State the blood parasite species.
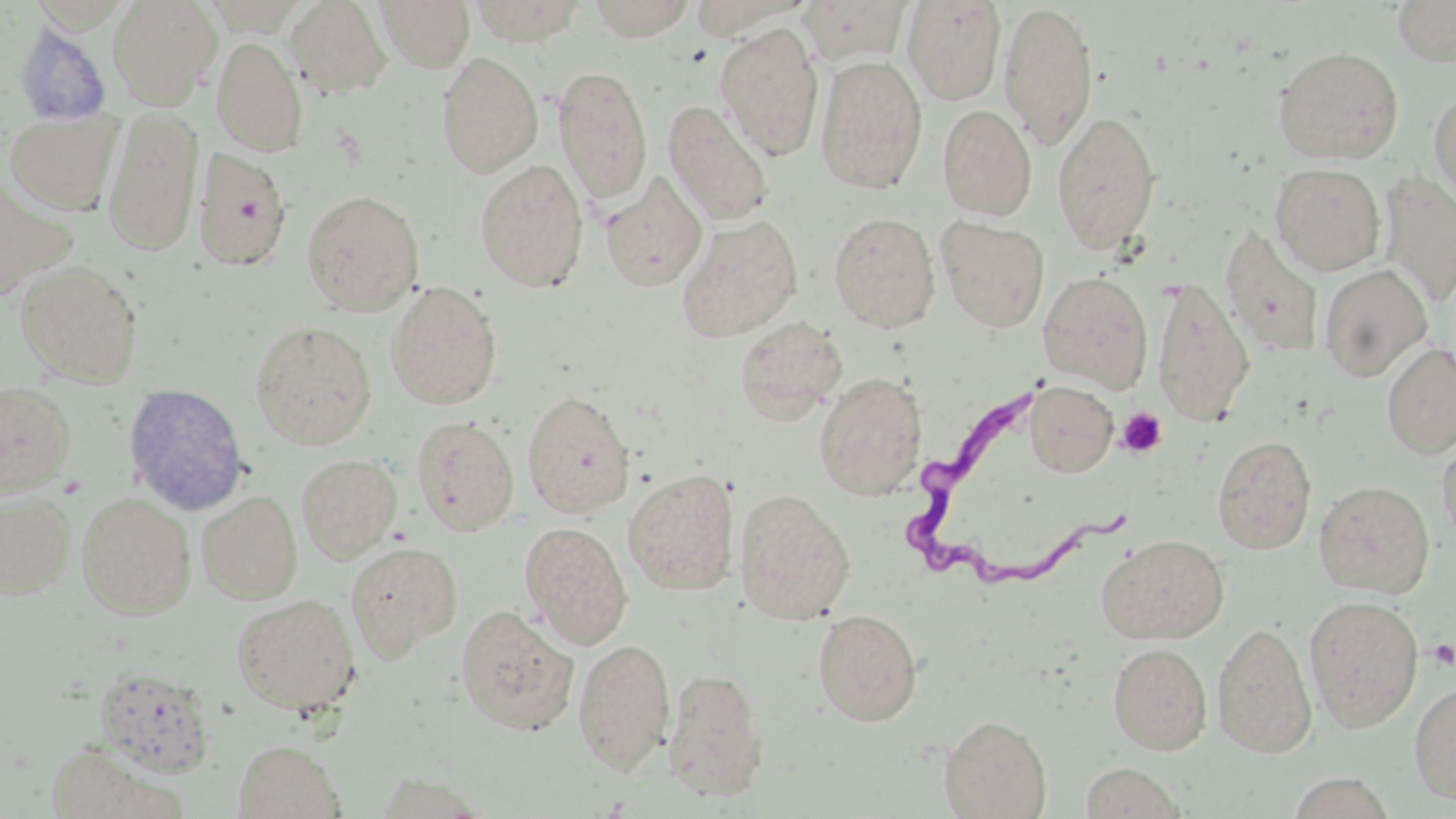
Trypanosoma brucei.

Approximate bounding boxes as (x1,y1)-(x2,y2) corner pairs in pixels. Platelet locations: (1117,407)-(1167,458), (1428,639)-(1456,669). Trypanosoma brucei locations: (904,381)-(1131,591). Uninfected red blood cell locations: (108,0)-(222,107), (284,0)-(392,100), (375,0)-(474,72), (469,0)-(589,44), (589,0)-(696,41), (800,0)-(911,65), (902,0)-(1007,105), (1392,0)-(1456,66), (999,2)-(1099,149), (14,14)-(223,121), (13,22)-(112,127), (715,22)-(825,159), (212,36)-(308,156), (1273,45)-(1404,164), (437,51)-(543,177), (815,55)-(928,194), (552,65)-(653,205), (1428,88)-(1456,207), (663,100)-(774,227), (937,104)-(1037,220), (103,107)-(203,256), (4,110)-(122,215), (1051,110)-(1162,253), (193,147)-(292,271), (474,159)-(589,291), (1270,162)-(1386,275), (1378,172)-(1456,307), (600,173)-(708,291), (301,189)-(425,315), (828,212)-(941,332), (677,214)-(803,342), (937,217)-(1050,332), (1220,225)-(1325,359), (15,260)-(143,388), (1319,265)-(1432,382), (1038,272)-(1153,392), (1152,276)-(1255,428), (385,281)-(503,410), (734,315)-(847,424), (250,320)-(377,449), (1381,342)-(1456,459), (814,372)-(928,500), (1026,381)-(1118,477), (0,382)-(76,497), (121,382)-(251,516), (522,389)-(636,517), (411,416)-(520,536), (1437,431)-(1456,550), (1212,435)-(1317,555), (296,454)-(402,563), (623,468)-(739,595), (1314,480)-(1435,598), (735,489)-(855,624), (0,491)-(77,598), (76,491)-(196,619), (197,491)-(303,604), (520,522)-(632,647), (1098,534)-(1230,644), (345,541)-(462,662), (231,593)-(360,715), (1304,595)-(1423,732), (455,603)-(579,735), (813,608)-(923,726), (1212,621)-(1317,757), (573,637)-(674,774), (1108,643)-(1212,754), (93,666)-(218,780), (664,667)-(768,800), (1409,679)-(1456,805), (939,715)-(1051,819), (43,738)-(179,819), (233,739)-(347,819), (1080,762)-(1186,818). May-Grünwald-Giemsa stain. Image is 1456×819 pixels. Thin blood smear. 1000x magnification. Single field of view. Optical microscopy.